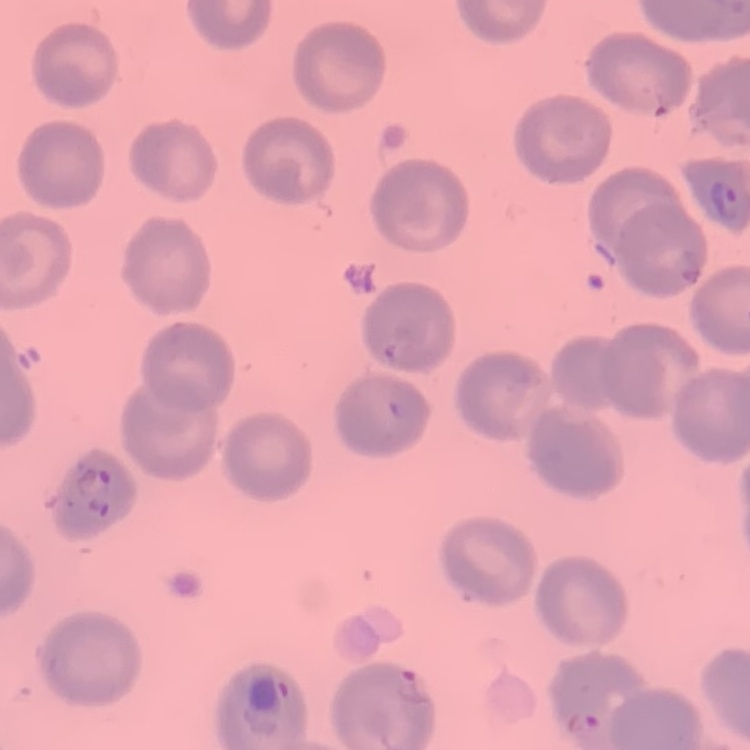
{
  "erythrocyte_morphology": "no rouleaux formation",
  "stain": "Field's or Giemsa",
  "preparation": "thin blood smear",
  "image_type": "square crop of a larger photomicrograph"
}